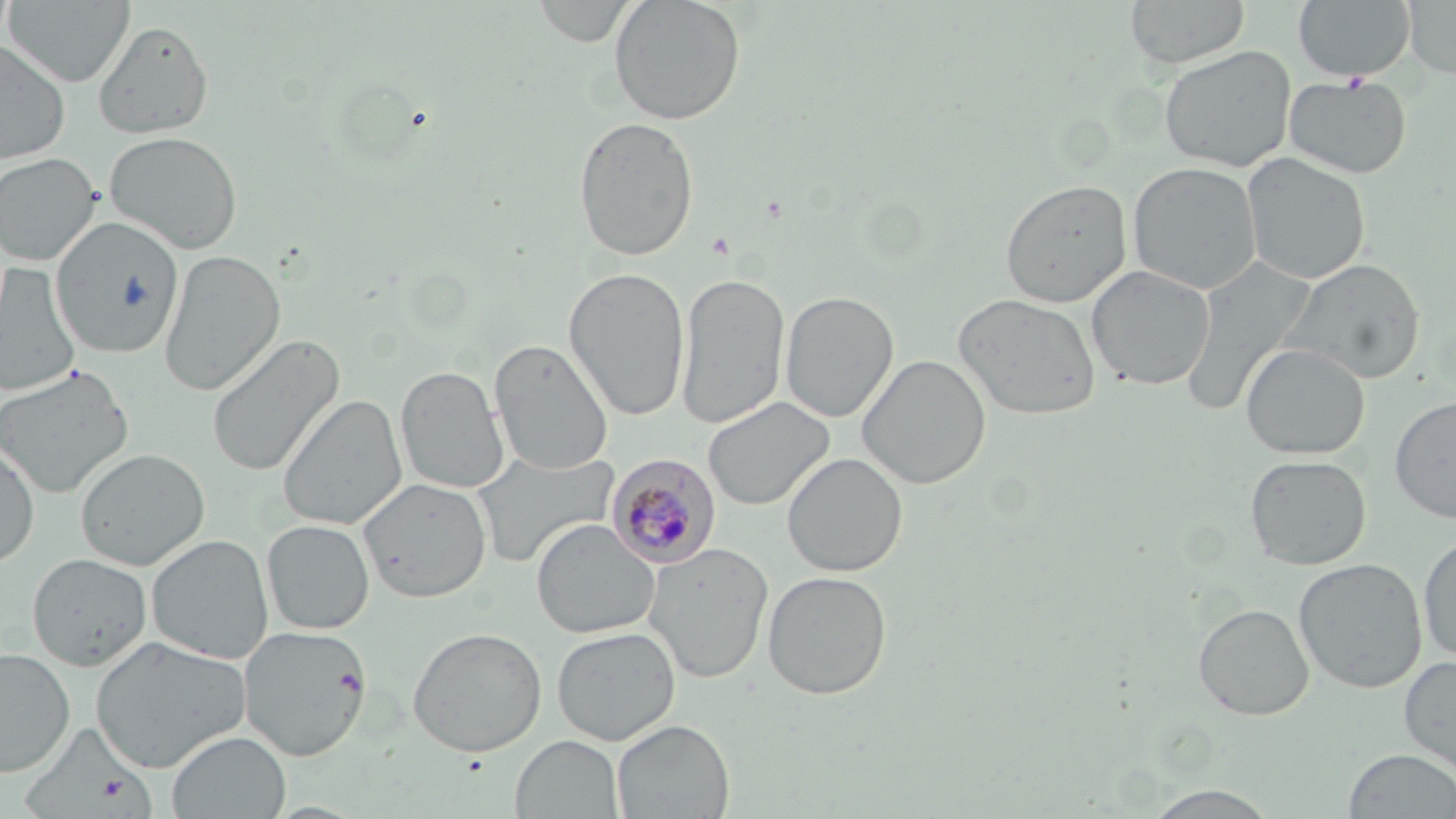

{
  "slide_level_diagnosis": "Plasmodium malariae",
  "image_size": "1456×819 pixels",
  "field_of_view": "single",
  "uninfected_red_blood_cell_locations": "approximate bounding boxes as (x1,y1)-(x2,y2) corner pairs in pixels: (4,0)-(136,88), (532,0)-(638,46), (608,0)-(746,125), (1124,0)-(1250,69), (1293,0)-(1416,81), (1402,0)-(1456,78), (93,19)-(215,140), (0,40)-(71,163), (0,42)-(85,264), (1159,45)-(1296,172), (1283,74)-(1413,179), (572,115)-(699,262), (104,130)-(244,254), (1241,152)-(1371,285), (0,153)-(100,265), (1128,162)-(1262,295), (1000,178)-(1132,308), (51,217)-(185,358), (159,249)-(286,395), (1281,257)-(1425,385), (1180,259)-(1312,415), (1,264)-(81,397), (1086,265)-(1216,390), (563,267)-(690,421), (675,272)-(790,431), (780,291)-(898,423), (953,292)-(1101,420), (206,333)-(346,477), (489,338)-(613,475), (1241,343)-(1370,459), (857,354)-(991,489), (0,365)-(134,500), (396,366)-(509,494), (277,394)-(407,530), (1390,395)-(1456,524), (703,396)-(833,511), (0,441)-(40,569), (75,448)-(210,571), (472,450)-(621,569), (782,452)-(907,577), (1245,454)-(1371,570), (358,476)-(492,603), (531,518)-(660,638), (262,519)-(375,634), (1417,532)-(1456,664), (146,534)-(273,664), (643,542)-(773,683), (27,552)-(152,670), (1293,558)-(1427,693), (762,570)-(892,700), (1193,603)-(1314,720), (239,625)-(372,761), (407,626)-(547,757), (551,627)-(680,745), (90,635)-(251,772), (0,648)-(75,777), (1399,654)-(1456,783), (612,719)-(735,819), (167,730)-(291,818), (510,734)-(624,819), (1343,749)-(1456,818), (1137,785)-(1284,819)",
  "modality": "optical microscopy",
  "preparation": "thin blood smear",
  "plasmodium_malariae_infected_red_blood_cell_locations": "approximate bounding boxes as (x1,y1)-(x2,y2) corner pairs in pixels: (606,454)-(721,569)",
  "stain": "May-Grünwald-Giemsa",
  "magnification": "1000x",
  "platelet_locations": "approximate bounding boxes as (x1,y1)-(x2,y2) corner pairs in pixels: (99,775)-(127,804)"
}